State which parasite is depicted.
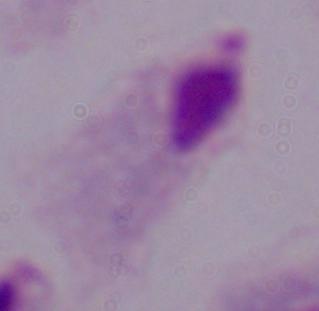
A trichomonad.

Summary:
  - Modality: photomicrograph
  - Magnification: 1000x